Comment on the morphology of the red blood cells.
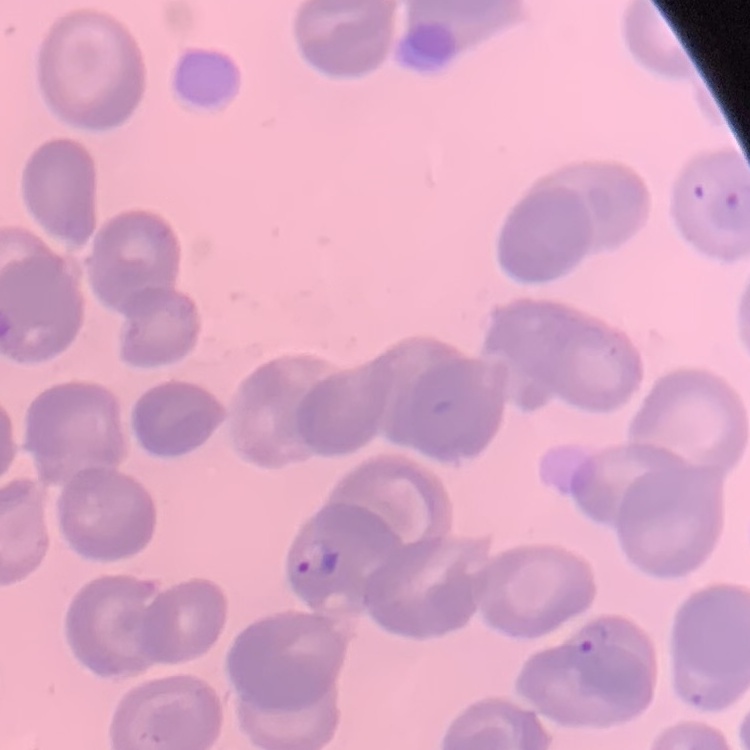
No rouleaux formation.

Square crop of a larger photomicrograph. Field's or Giemsa stain. Thin blood smear.